Report the malaria status of this cell.
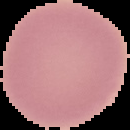
It is uninfected.

image_type: cell region segmented out of the field of view; surrounding area masked to black
image_size: 130×130 pixels
preparation: thin blood film